Assess this cell for malaria.
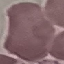

Uninfected.

capture = smartphone camera at the microscope eyepiece
stain = Giemsa
preparation = thin smear
image type = cell patch, automatically extracted from a larger field of view and resized to 64 × 64 pixels